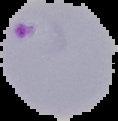
image_size: 118×121 pixels
image_type: segmented cell region on a black background
preparation: thin blood smear
result: malaria parasites identified